Give the preparation type.
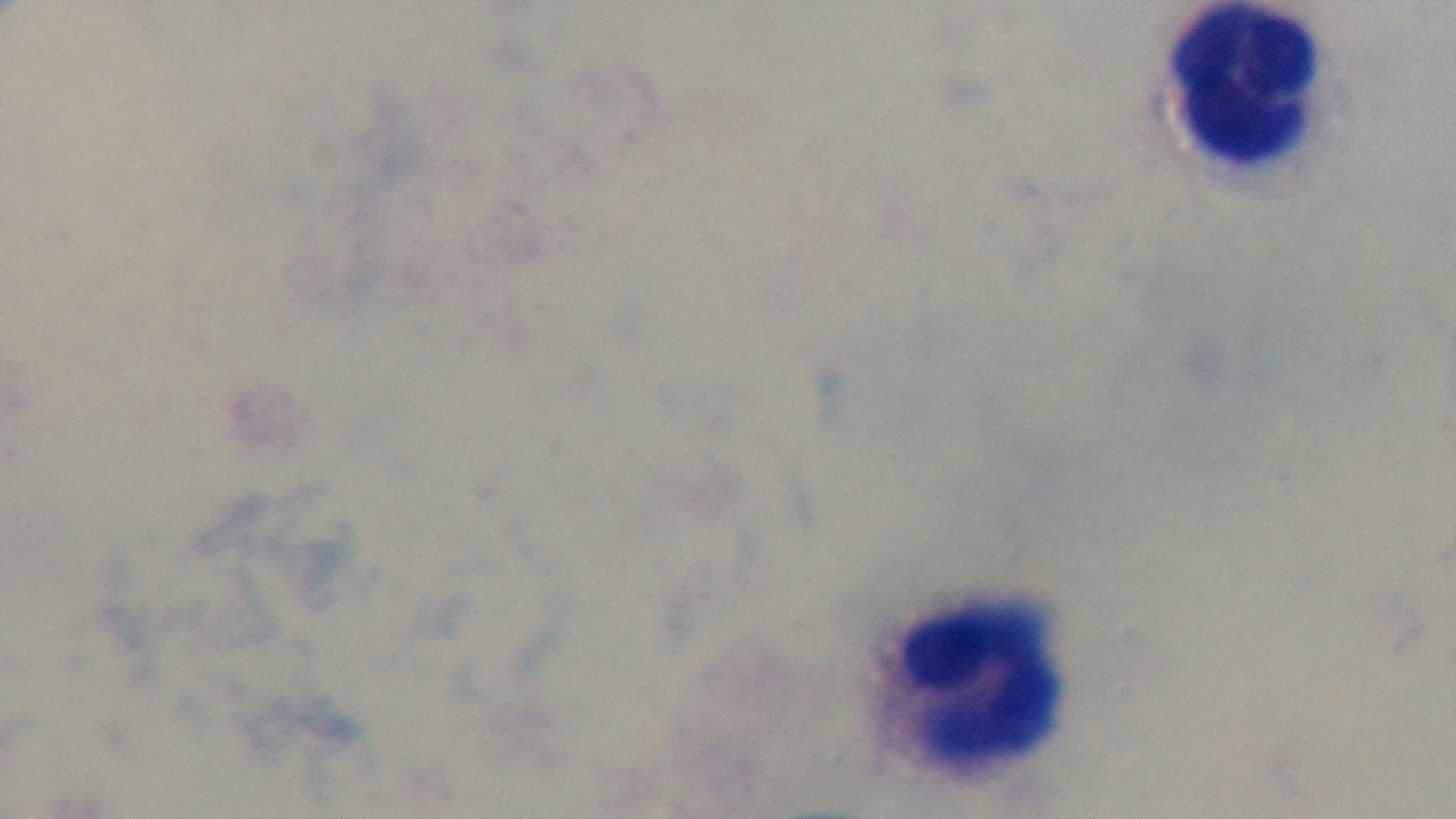
Thick.

Malaria status: uninfected. Photomicrograph. One field from the slide. 100x oil-immersion objective. Giemsa stain. Mounted 4K digital camera.